Describe the morphology of the red blood cells.
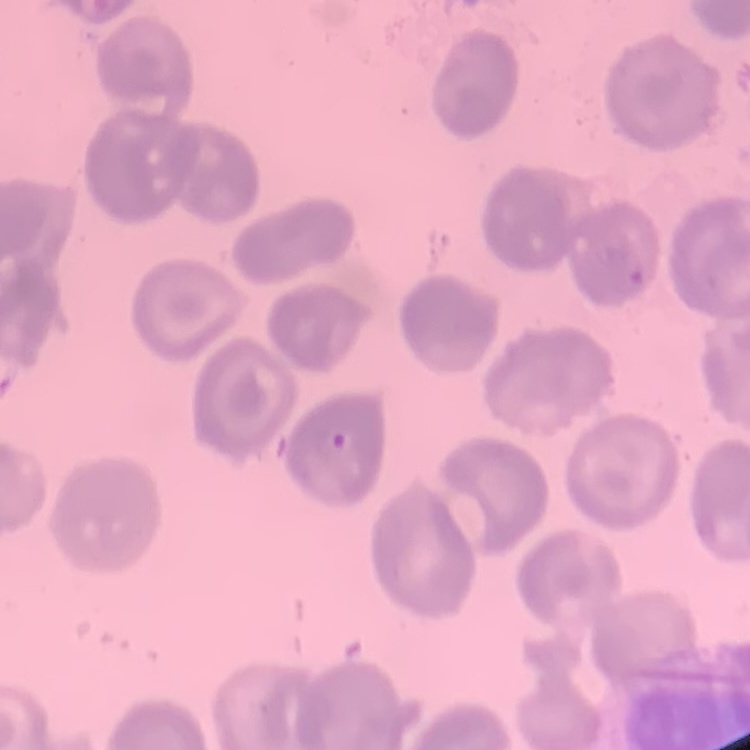
No rouleaux formation.

Summary:
  - Image type: one tile cut from a larger photomicrograph
  - Preparation: thin blood film
  - Stain: Field's or Giemsa